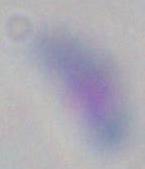
Summary:
  - Modality: photomicrograph
  - Identification: Toxoplasma gondii
  - Magnification: 1000x